Locate and identify every blood parasite.
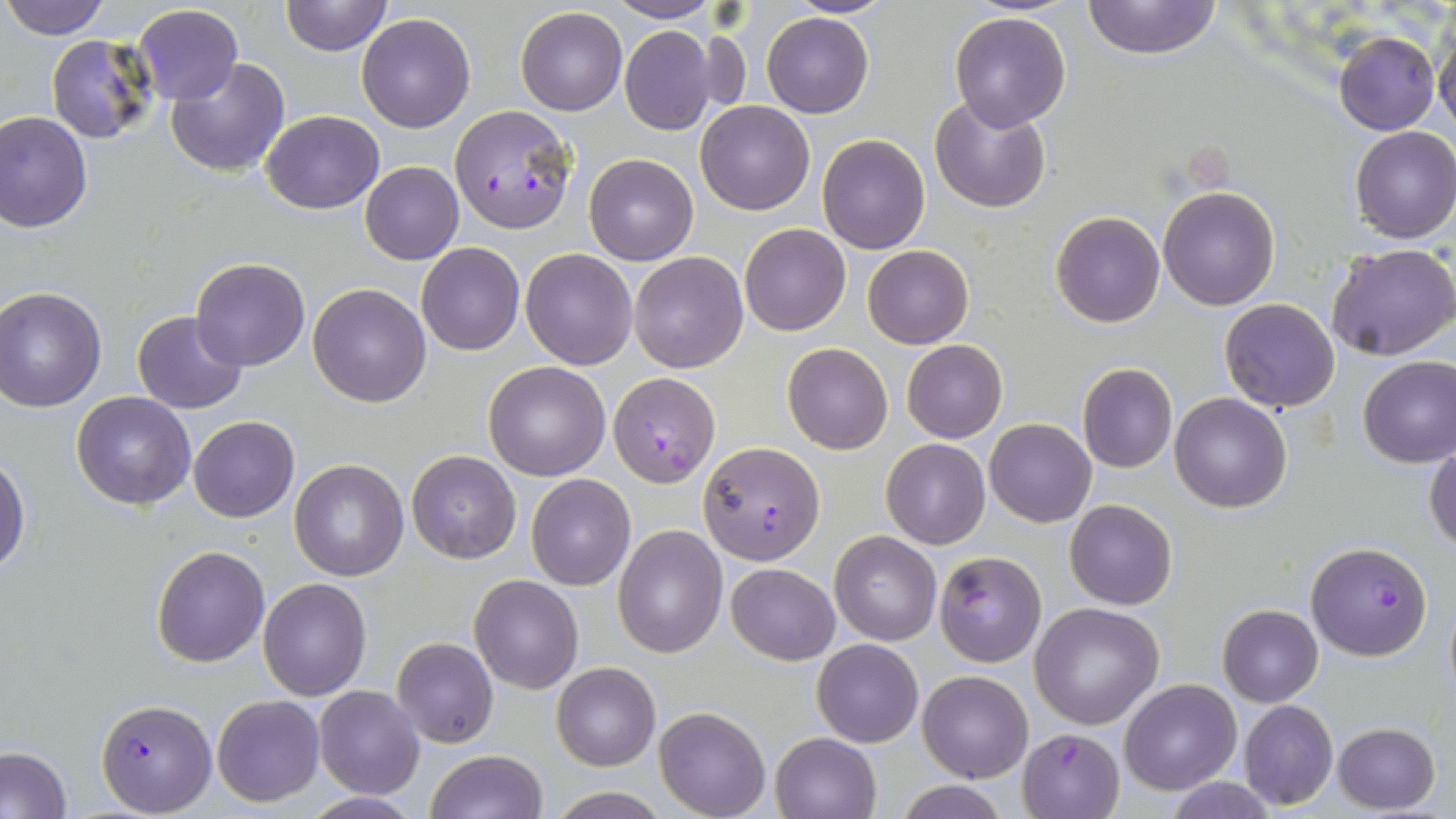

Approximate bounding boxes as (x1, y1, x2, y2) in pixels.
Plasmodium falciparum-infected red blood cells: (450, 104, 577, 233), (608, 371, 721, 488), (697, 441, 826, 565), (1306, 540, 1432, 659), (934, 551, 1047, 666), (94, 698, 217, 815), (1018, 728, 1124, 818).
No Plasmodium ovale, Plasmodium malariae, Plasmodium vivax, Babesia divergens, or Trypanosoma brucei observed.

Summary:
  - Uninfected red blood cell locations: (1, 0, 112, 39), (783, 0, 899, 18), (1083, 0, 1222, 60), (279, 1, 391, 56), (604, 1, 720, 23), (133, 3, 242, 104), (515, 7, 627, 116), (948, 11, 1072, 131), (357, 12, 475, 132), (762, 12, 874, 119), (1434, 22, 1456, 133), (619, 25, 719, 134), (1334, 30, 1439, 136), (45, 33, 161, 145), (165, 57, 291, 175), (930, 95, 1052, 213), (697, 101, 815, 216), (261, 109, 383, 213), (0, 110, 94, 232), (1350, 127, 1456, 244), (818, 133, 930, 254), (584, 153, 697, 265), (360, 162, 464, 265), (1158, 186, 1280, 310), (1050, 209, 1166, 328), (739, 223, 852, 337), (417, 242, 525, 355), (1328, 244, 1456, 361), (862, 245, 974, 349), (520, 248, 637, 369), (628, 251, 749, 373), (189, 257, 310, 371), (308, 282, 432, 407), (0, 287, 107, 411), (1219, 298, 1340, 412), (132, 310, 249, 414), (900, 339, 1007, 444), (782, 343, 893, 454), (1357, 355, 1456, 468), (483, 361, 610, 480), (1077, 362, 1178, 474), (73, 392, 196, 511), (1169, 392, 1293, 512), (189, 416, 299, 522), (985, 418, 1096, 527), (882, 439, 990, 549), (1424, 441, 1456, 552), (406, 449, 522, 564), (0, 453, 30, 576), (290, 459, 409, 581), (526, 474, 636, 591), (1064, 499, 1178, 610), (612, 525, 727, 658), (830, 531, 941, 645), (152, 545, 270, 666), (727, 562, 840, 665), (468, 573, 584, 693), (258, 577, 372, 700), (1442, 583, 1456, 707), (1030, 602, 1164, 730), (1217, 605, 1323, 707), (392, 637, 498, 747), (810, 638, 925, 747), (551, 662, 660, 770), (918, 671, 1033, 783), (1120, 678, 1241, 795), (314, 685, 426, 799), (211, 694, 323, 806), (1237, 699, 1338, 810), (655, 707, 771, 819), (1333, 722, 1441, 814), (770, 732, 880, 819), (0, 746, 73, 819), (424, 749, 546, 819), (1164, 777, 1277, 817), (890, 779, 1015, 818), (548, 788, 668, 819), (302, 792, 423, 819)
  - Slide-level diagnosis: Plasmodium falciparum
  - Modality: optical microscopy
  - Image size: 1456×819 pixels
  - Preparation: thin blood smear
  - Magnification: 1000x
  - Stain: May-Grünwald-Giemsa
  - Field of view: one of a larger specimen